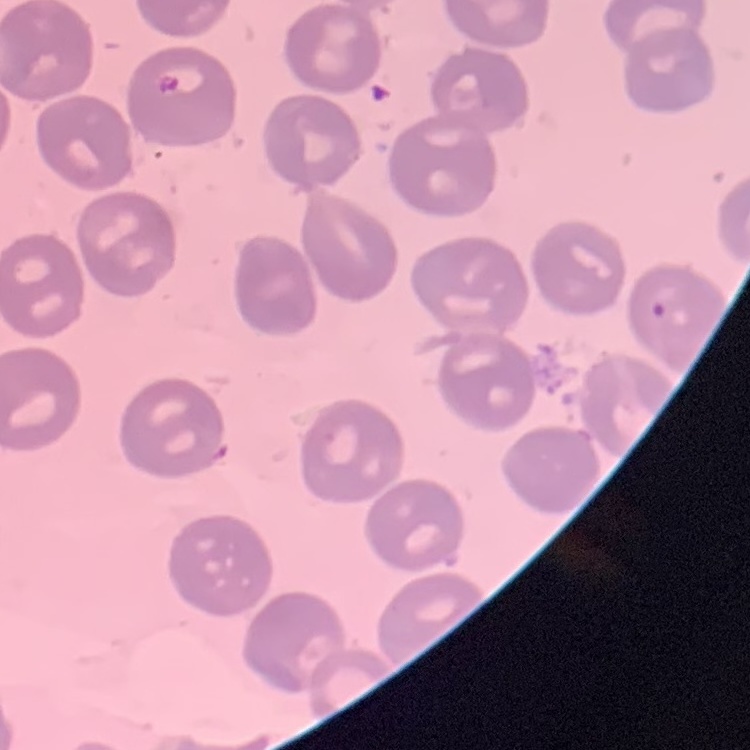

red_blood_cell_morphology: no rouleaux formation
image_type: one tile cut from a larger photomicrograph
preparation: thin blood film
stain: Field's or Giemsa